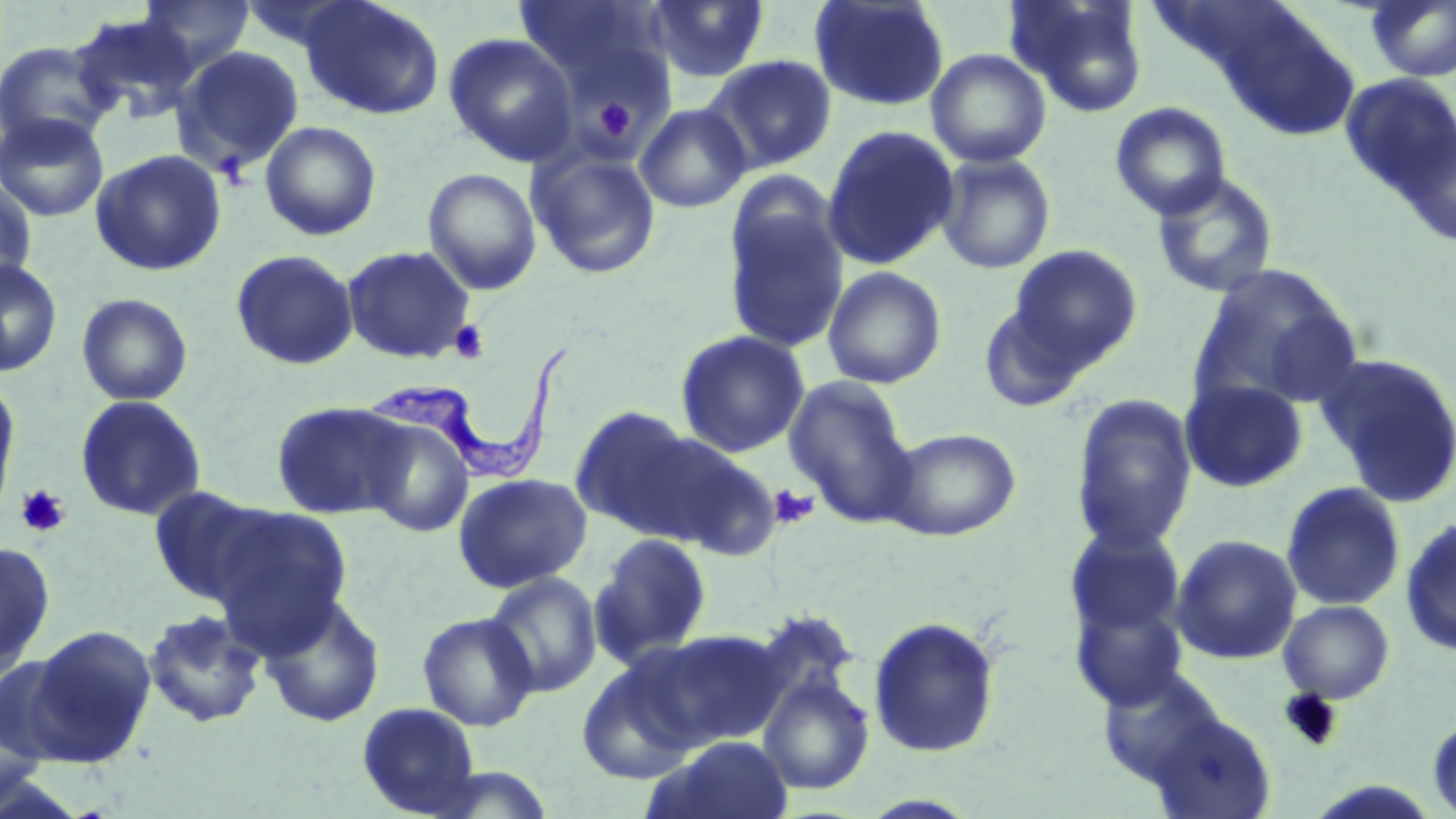
Trypanosoma brucei locations = approximate bounding boxes as (x1, y1, x2, y2) in pixels: (363, 347, 568, 484)
slide-level diagnosis = Trypanosoma brucei
uninfected red blood cell locations = approximate bounding boxes as (x1, y1, x2, y2) in pixels: (138, 0, 255, 74), (239, 0, 365, 54), (298, 0, 444, 120), (514, 0, 670, 93), (645, 0, 771, 83), (1006, 0, 1151, 118), (809, 1, 950, 112), (1366, 1, 1456, 82), (71, 13, 200, 125), (443, 33, 578, 167), (0, 39, 115, 150), (173, 46, 305, 175), (926, 48, 1052, 168), (703, 55, 837, 174), (1339, 73, 1456, 202), (1110, 102, 1232, 220), (634, 103, 752, 213), (0, 111, 109, 222), (259, 120, 382, 241), (1394, 122, 1455, 249), (821, 126, 958, 270), (527, 146, 662, 280), (90, 149, 226, 276), (935, 153, 1056, 275), (422, 167, 542, 295), (1151, 172, 1280, 298), (0, 179, 37, 293), (722, 190, 849, 354), (1007, 244, 1143, 370), (341, 245, 476, 364), (230, 249, 359, 370), (0, 259, 63, 377), (1188, 264, 1363, 414), (822, 266, 947, 389), (76, 293, 193, 406), (977, 297, 1094, 414), (675, 329, 811, 458), (1314, 351, 1456, 508), (783, 374, 919, 527), (0, 376, 21, 530), (1180, 378, 1309, 493), (1069, 393, 1197, 552), (75, 395, 207, 521), (270, 400, 410, 519), (568, 404, 710, 539), (361, 416, 476, 538), (885, 427, 1022, 541), (654, 438, 785, 562), (453, 473, 593, 593), (1280, 481, 1406, 612), (148, 485, 276, 607), (208, 504, 354, 649), (1400, 514, 1456, 656), (1064, 524, 1186, 640), (590, 532, 713, 667), (1170, 534, 1303, 665), (0, 540, 55, 676), (483, 571, 603, 699), (259, 591, 386, 729), (1070, 595, 1192, 710), (1277, 599, 1395, 704), (142, 608, 266, 729), (417, 611, 539, 731), (867, 614, 1002, 759), (29, 624, 157, 763), (636, 630, 788, 752), (2, 649, 85, 766), (575, 657, 704, 786), (1096, 667, 1228, 788), (757, 671, 875, 795), (1, 699, 50, 812), (356, 701, 481, 817), (1145, 708, 1278, 819), (1426, 711, 1456, 817), (660, 735, 794, 819)
platelet locations = approximate bounding boxes as (x1, y1, x2, y2) in pixels: (592, 95, 639, 143), (448, 319, 490, 363), (16, 485, 70, 537), (770, 485, 818, 530)
image size = 1456×819 pixels
preparation = thin blood film
modality = light microscopy
stain = May-Grünwald-Giemsa
field of view = single
magnification = 1000x